Find the red blood cells that are infected with P. falciparum, and any of indeterminate infection status.
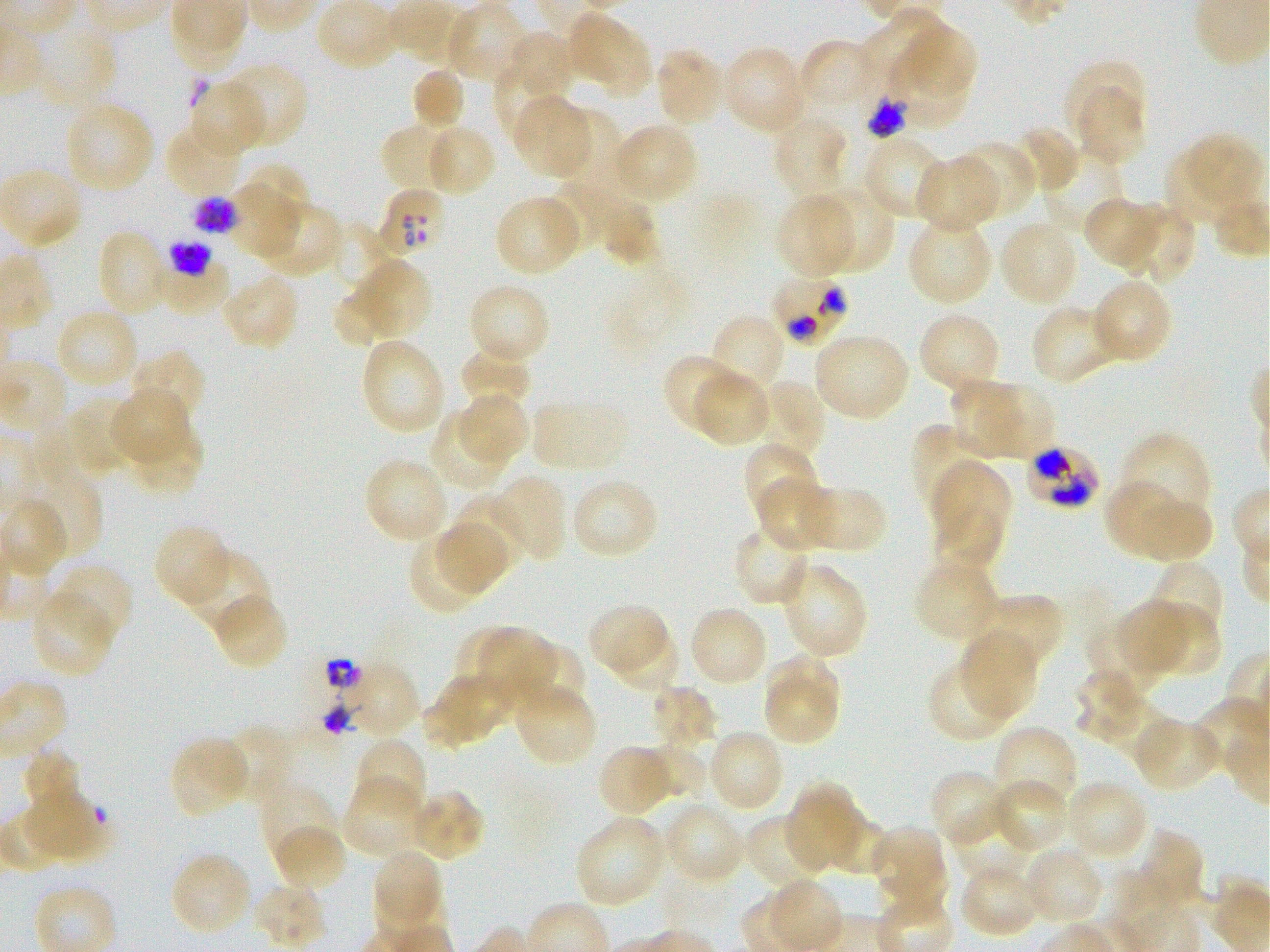

Approximate bounding boxes as (x1, y1, x2, y2) in pixels. Not every red blood cell is marked. A life-cycle stage — or a range of stages, where the recorded stages span more than one — follows each staged infected red blood cell.
Infected red blood cells: (378, 187, 447, 258); (192, 195, 238, 236) early trophozoite to late schizont; (775, 280, 847, 347); (1027, 449, 1097, 506).
Red blood cells of indeterminate infection status: (867, 90, 909, 139), (156, 242, 228, 314).

Summary:
  - Locations of uninfected red blood cells: (445, 3, 527, 84), (858, 8, 949, 95), (568, 13, 633, 84), (31, 17, 118, 108), (896, 23, 977, 100), (504, 31, 576, 99), (601, 34, 649, 99), (798, 38, 877, 109), (720, 46, 810, 134), (654, 48, 725, 126), (890, 48, 969, 131), (1063, 59, 1146, 141), (493, 61, 563, 140), (222, 62, 307, 147), (410, 68, 466, 132), (189, 79, 265, 157), (1076, 88, 1145, 167), (512, 94, 591, 178), (63, 100, 154, 192), (557, 107, 623, 185), (773, 116, 848, 197), (380, 121, 461, 194), (612, 123, 698, 203), (1014, 123, 1080, 193), (165, 124, 245, 196), (425, 124, 497, 197), (862, 135, 946, 219), (1181, 135, 1261, 214), (956, 141, 1036, 220), (1164, 147, 1238, 227), (1042, 151, 1125, 233), (913, 155, 999, 234), (241, 164, 310, 226), (549, 180, 628, 249), (226, 181, 298, 260), (813, 185, 894, 274), (774, 193, 855, 277), (494, 194, 582, 276), (1083, 197, 1161, 270), (256, 201, 342, 278), (598, 201, 660, 266), (1123, 204, 1196, 284), (906, 216, 994, 304), (327, 220, 391, 290), (999, 220, 1079, 307), (96, 229, 171, 318), (352, 259, 433, 338), (220, 273, 300, 351), (1092, 277, 1173, 363), (466, 283, 551, 365), (331, 289, 388, 347), (1030, 304, 1123, 385), (55, 308, 139, 390), (917, 311, 1002, 396), (710, 314, 785, 398), (813, 332, 911, 420), (361, 337, 447, 435), (459, 344, 534, 409), (128, 350, 206, 427), (661, 352, 743, 434), (692, 370, 772, 447), (950, 376, 1022, 457), (758, 381, 827, 462), (982, 381, 1053, 458), (111, 388, 189, 466), (457, 393, 529, 466), (67, 397, 136, 477), (532, 397, 629, 473), (36, 412, 100, 488), (429, 412, 508, 491), (128, 422, 204, 496), (911, 423, 988, 512), (1121, 432, 1212, 519), (743, 441, 819, 524), (364, 456, 449, 545), (932, 460, 1010, 547), (33, 475, 102, 559), (493, 475, 568, 561), (571, 476, 660, 560), (754, 477, 834, 553), (1104, 480, 1187, 557), (803, 484, 887, 554), (1128, 491, 1213, 563), (451, 494, 525, 575), (933, 502, 1004, 571), (434, 520, 510, 595), (153, 523, 232, 606), (733, 525, 811, 605), (408, 532, 486, 616), (183, 551, 272, 639), (912, 560, 1000, 642), (1148, 561, 1225, 641), (781, 562, 870, 660), (52, 563, 134, 644), (31, 591, 116, 678), (979, 593, 1064, 671), (212, 594, 287, 671), (1116, 600, 1192, 674), (1141, 602, 1221, 676), (588, 603, 666, 676), (689, 605, 768, 687), (1086, 620, 1165, 696), (459, 625, 533, 712), (610, 625, 679, 692), (481, 626, 557, 709), (960, 631, 1038, 718), (518, 643, 588, 714), (763, 660, 841, 744), (927, 660, 1015, 743), (342, 661, 421, 739), (1073, 668, 1145, 740), (424, 673, 509, 748), (513, 684, 598, 766), (649, 685, 719, 751), (1106, 698, 1173, 762), (1133, 717, 1221, 791), (221, 723, 293, 799), (993, 724, 1078, 811), (708, 729, 785, 812), (170, 736, 250, 819), (354, 737, 427, 816), (645, 744, 705, 800), (596, 745, 674, 817), (21, 748, 84, 823), (928, 768, 1011, 847), (341, 777, 422, 858), (991, 777, 1069, 854), (1065, 780, 1148, 861), (258, 783, 337, 866), (788, 784, 860, 870), (407, 789, 486, 862), (24, 791, 107, 860), (663, 802, 745, 885), (824, 808, 890, 875), (950, 812, 1032, 883), (745, 814, 829, 893), (574, 816, 667, 909), (272, 824, 347, 894), (871, 826, 943, 895), (1135, 830, 1205, 914), (1021, 848, 1104, 926), (372, 849, 442, 922), (170, 852, 251, 936), (959, 861, 1041, 939), (252, 883, 327, 949)
  - Preparation: thin blood smear
  - Donor blood group: O+
  - Field of view: single
  - Image size: 1270×952 pixels
  - Objective: 100x, oil immersion, numerical aperture 1.25
  - Culture: in-vitro P. falciparum strain 3D7, static
  - Stain: Giemsa